State the blood parasite species.
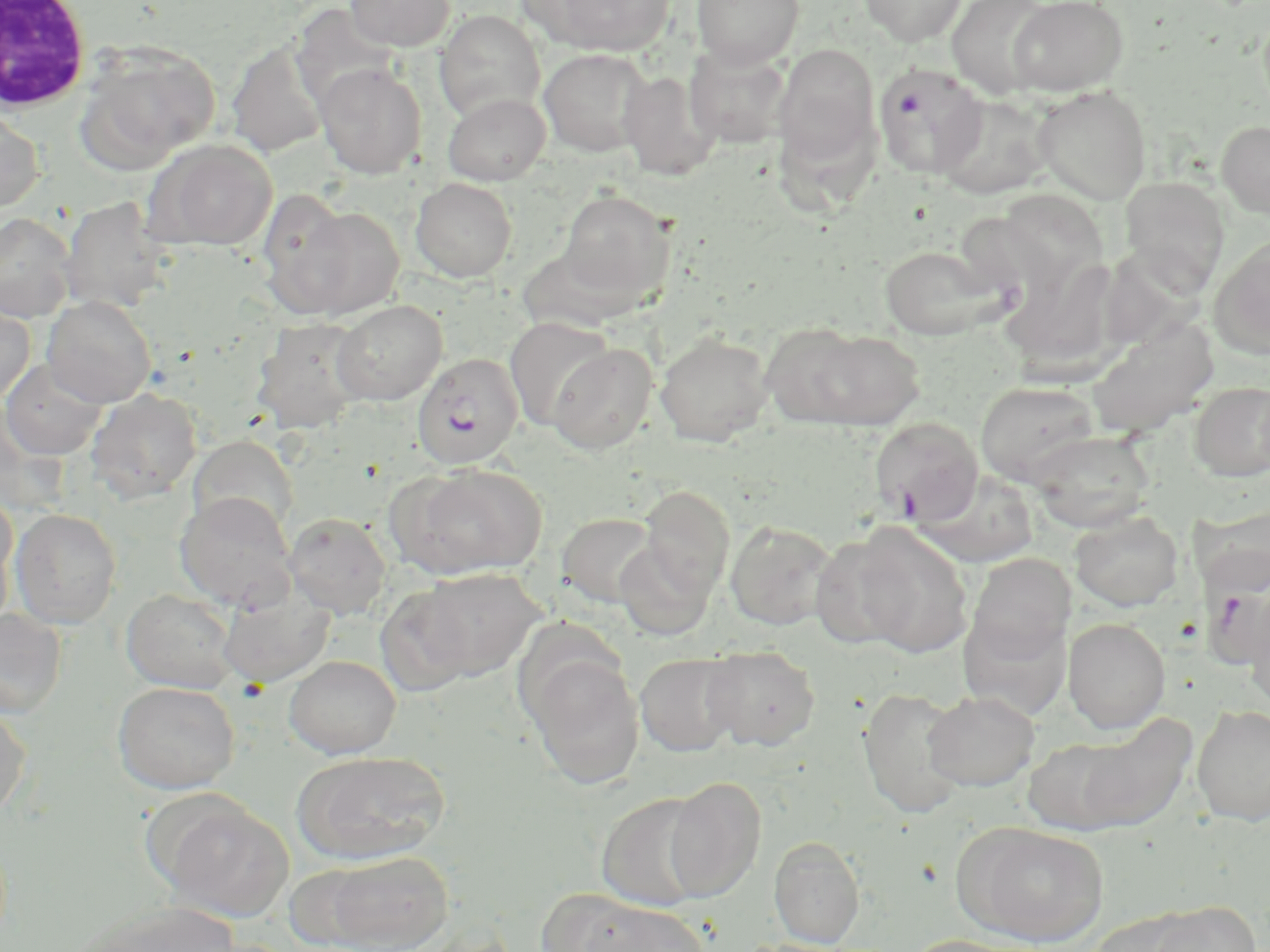

Plasmodium falciparum.

Summary:
  - Coordinate format: approximate bounding boxes as named x1/y1/x2/y2 corners in pixels
  - White blood cell locations: (x1=0, y1=1, x2=92, y2=114)
  - Uninfected red blood cell locations: (x1=346, y1=0, x2=455, y2=51), (x1=529, y1=0, x2=675, y2=57), (x1=692, y1=0, x2=804, y2=67), (x1=859, y1=0, x2=968, y2=46), (x1=946, y1=0, x2=1056, y2=100), (x1=1008, y1=0, x2=1128, y2=96), (x1=434, y1=10, x2=545, y2=123), (x1=226, y1=40, x2=328, y2=158), (x1=772, y1=42, x2=881, y2=169), (x1=76, y1=43, x2=221, y2=171), (x1=684, y1=44, x2=792, y2=148), (x1=538, y1=48, x2=654, y2=157), (x1=315, y1=63, x2=426, y2=179), (x1=618, y1=71, x2=719, y2=181), (x1=1032, y1=85, x2=1152, y2=205), (x1=443, y1=92, x2=550, y2=185), (x1=934, y1=93, x2=1053, y2=200), (x1=0, y1=106, x2=45, y2=212), (x1=777, y1=109, x2=897, y2=225), (x1=1216, y1=120, x2=1270, y2=219), (x1=146, y1=139, x2=278, y2=251), (x1=998, y1=173, x2=1115, y2=303), (x1=1119, y1=176, x2=1230, y2=292), (x1=410, y1=177, x2=517, y2=282), (x1=256, y1=187, x2=356, y2=309), (x1=557, y1=189, x2=676, y2=306), (x1=60, y1=196, x2=173, y2=313), (x1=286, y1=205, x2=405, y2=320), (x1=0, y1=212, x2=77, y2=322), (x1=1209, y1=237, x2=1270, y2=361), (x1=878, y1=245, x2=1003, y2=340), (x1=1000, y1=255, x2=1149, y2=382), (x1=42, y1=295, x2=156, y2=407), (x1=0, y1=299, x2=36, y2=403), (x1=331, y1=300, x2=447, y2=405), (x1=504, y1=316, x2=617, y2=431), (x1=251, y1=317, x2=369, y2=433), (x1=1085, y1=318, x2=1219, y2=438), (x1=760, y1=322, x2=873, y2=427), (x1=807, y1=330, x2=925, y2=429), (x1=655, y1=331, x2=775, y2=446), (x1=546, y1=343, x2=657, y2=455), (x1=1, y1=359, x2=109, y2=461), (x1=1188, y1=380, x2=1270, y2=482), (x1=975, y1=381, x2=1100, y2=487), (x1=86, y1=389, x2=202, y2=504), (x1=1028, y1=430, x2=1156, y2=532), (x1=188, y1=435, x2=298, y2=539), (x1=399, y1=463, x2=547, y2=579), (x1=915, y1=469, x2=1040, y2=568), (x1=640, y1=486, x2=735, y2=599), (x1=174, y1=491, x2=296, y2=611), (x1=0, y1=494, x2=18, y2=617), (x1=1184, y1=500, x2=1270, y2=595), (x1=10, y1=508, x2=121, y2=629), (x1=1070, y1=511, x2=1183, y2=611), (x1=556, y1=512, x2=658, y2=609), (x1=284, y1=513, x2=392, y2=619), (x1=724, y1=520, x2=839, y2=631), (x1=846, y1=523, x2=974, y2=657), (x1=809, y1=533, x2=920, y2=654), (x1=613, y1=540, x2=715, y2=641), (x1=966, y1=553, x2=1073, y2=668), (x1=415, y1=567, x2=544, y2=681), (x1=1243, y1=581, x2=1270, y2=712), (x1=375, y1=583, x2=478, y2=698), (x1=217, y1=585, x2=335, y2=689), (x1=121, y1=588, x2=240, y2=693), (x1=958, y1=600, x2=1071, y2=720), (x1=0, y1=608, x2=68, y2=718), (x1=1063, y1=618, x2=1170, y2=734), (x1=701, y1=645, x2=820, y2=751), (x1=521, y1=651, x2=646, y2=790), (x1=636, y1=653, x2=742, y2=756), (x1=284, y1=655, x2=401, y2=759), (x1=111, y1=681, x2=240, y2=794), (x1=857, y1=687, x2=969, y2=820), (x1=923, y1=691, x2=1039, y2=791), (x1=0, y1=702, x2=31, y2=822), (x1=1192, y1=705, x2=1270, y2=825), (x1=1070, y1=714, x2=1197, y2=833), (x1=1024, y1=735, x2=1138, y2=835), (x1=291, y1=749, x2=450, y2=865), (x1=663, y1=777, x2=766, y2=902), (x1=595, y1=792, x2=713, y2=912), (x1=153, y1=795, x2=294, y2=923), (x1=958, y1=822, x2=1109, y2=946), (x1=768, y1=836, x2=865, y2=947), (x1=314, y1=850, x2=453, y2=952), (x1=537, y1=888, x2=648, y2=951), (x1=72, y1=900, x2=242, y2=952), (x1=581, y1=900, x2=707, y2=952), (x1=1146, y1=901, x2=1261, y2=952), (x1=1085, y1=909, x2=1203, y2=951), (x1=898, y1=935, x2=1030, y2=952)
  - Plasmodium falciparum-infected red blood cell locations: (x1=874, y1=64, x2=988, y2=180), (x1=413, y1=353, x2=525, y2=468), (x1=870, y1=418, x2=983, y2=525)
  - Image size: 1270×952 pixels
  - Field of view: single
  - Preparation: thin blood film
  - Stain: May-Grünwald-Giemsa
  - Modality: optical microscopy
  - Magnification: 1000x